Outline platelets.
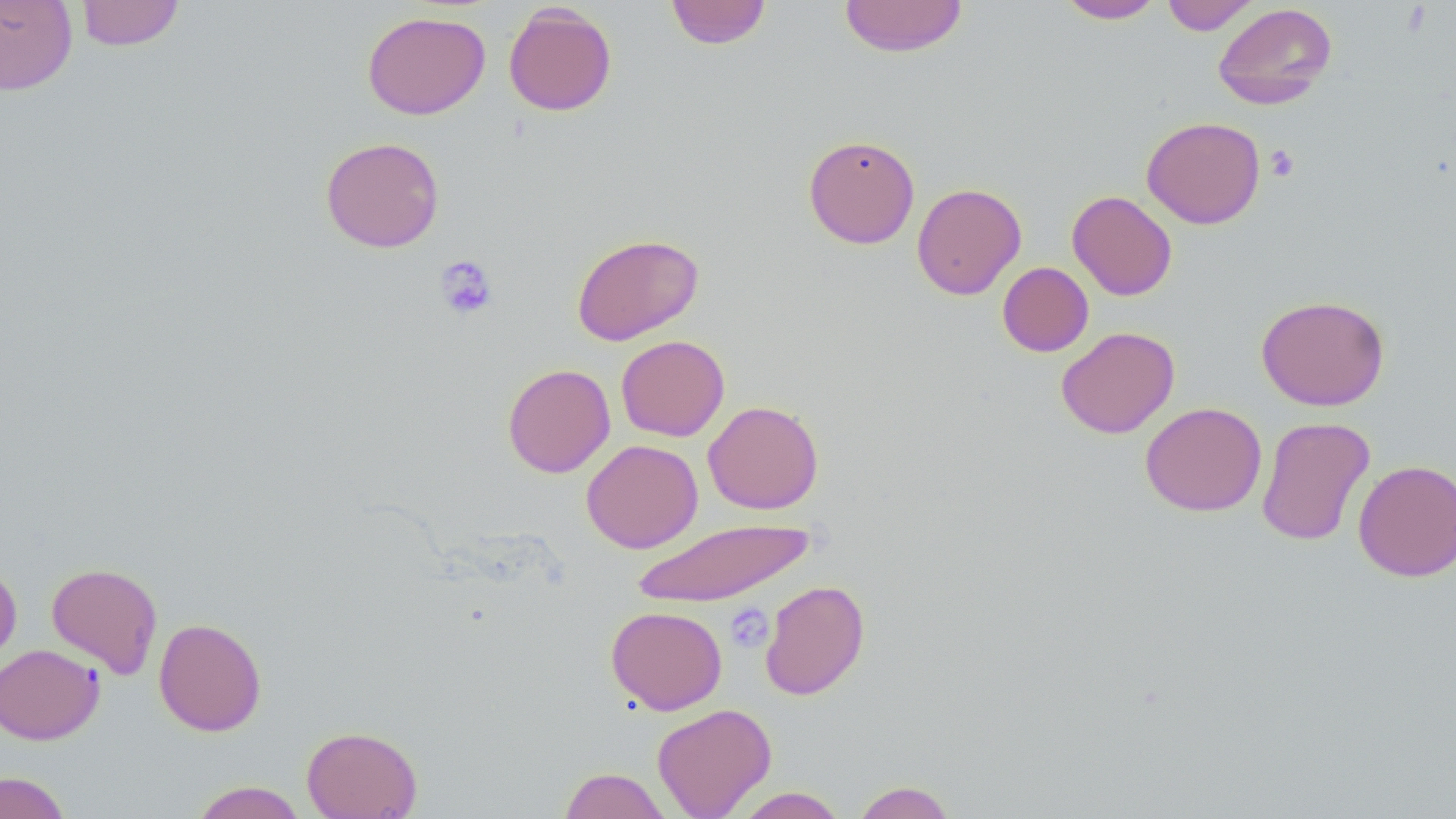

Approximate bounding boxes as named x1/y1/x2/y2 corners in pixels.
Platelets: (x1=1264, y1=144, x2=1300, y2=182), (x1=435, y1=255, x2=498, y2=320), (x1=725, y1=603, x2=773, y2=652).

Uninfected red blood cell locations: (x1=0, y1=0, x2=78, y2=95), (x1=665, y1=0, x2=772, y2=49), (x1=839, y1=0, x2=969, y2=58), (x1=1056, y1=0, x2=1165, y2=24), (x1=1161, y1=0, x2=1259, y2=35), (x1=75, y1=1, x2=185, y2=51), (x1=1213, y1=3, x2=1338, y2=110), (x1=503, y1=4, x2=617, y2=116), (x1=362, y1=11, x2=490, y2=119), (x1=1141, y1=116, x2=1265, y2=229), (x1=803, y1=134, x2=920, y2=249), (x1=320, y1=136, x2=445, y2=253), (x1=912, y1=182, x2=1026, y2=300), (x1=1067, y1=190, x2=1177, y2=301), (x1=571, y1=233, x2=704, y2=345), (x1=997, y1=262, x2=1094, y2=357), (x1=1256, y1=294, x2=1390, y2=411), (x1=1056, y1=326, x2=1180, y2=439), (x1=616, y1=335, x2=730, y2=441), (x1=502, y1=363, x2=615, y2=478), (x1=703, y1=400, x2=824, y2=515), (x1=1140, y1=402, x2=1267, y2=517), (x1=1256, y1=416, x2=1375, y2=547), (x1=581, y1=439, x2=703, y2=553), (x1=1353, y1=459, x2=1455, y2=581), (x1=631, y1=519, x2=815, y2=607), (x1=0, y1=560, x2=22, y2=670), (x1=46, y1=562, x2=163, y2=678), (x1=759, y1=579, x2=870, y2=700), (x1=606, y1=606, x2=727, y2=714), (x1=153, y1=617, x2=267, y2=736), (x1=0, y1=644, x2=104, y2=745), (x1=652, y1=702, x2=777, y2=818), (x1=301, y1=725, x2=422, y2=818), (x1=559, y1=767, x2=672, y2=819), (x1=0, y1=771, x2=71, y2=819), (x1=852, y1=780, x2=958, y2=819), (x1=190, y1=781, x2=307, y2=819), (x1=733, y1=787, x2=847, y2=818). Slide-level diagnosis: negative for blood parasites. Thin blood smear. One field of a larger specimen. 1000x magnification. Image is 1456×819 pixels. Optical microscopy. May-Grünwald-Giemsa-stained preparation.